Identify the blood parasite species.
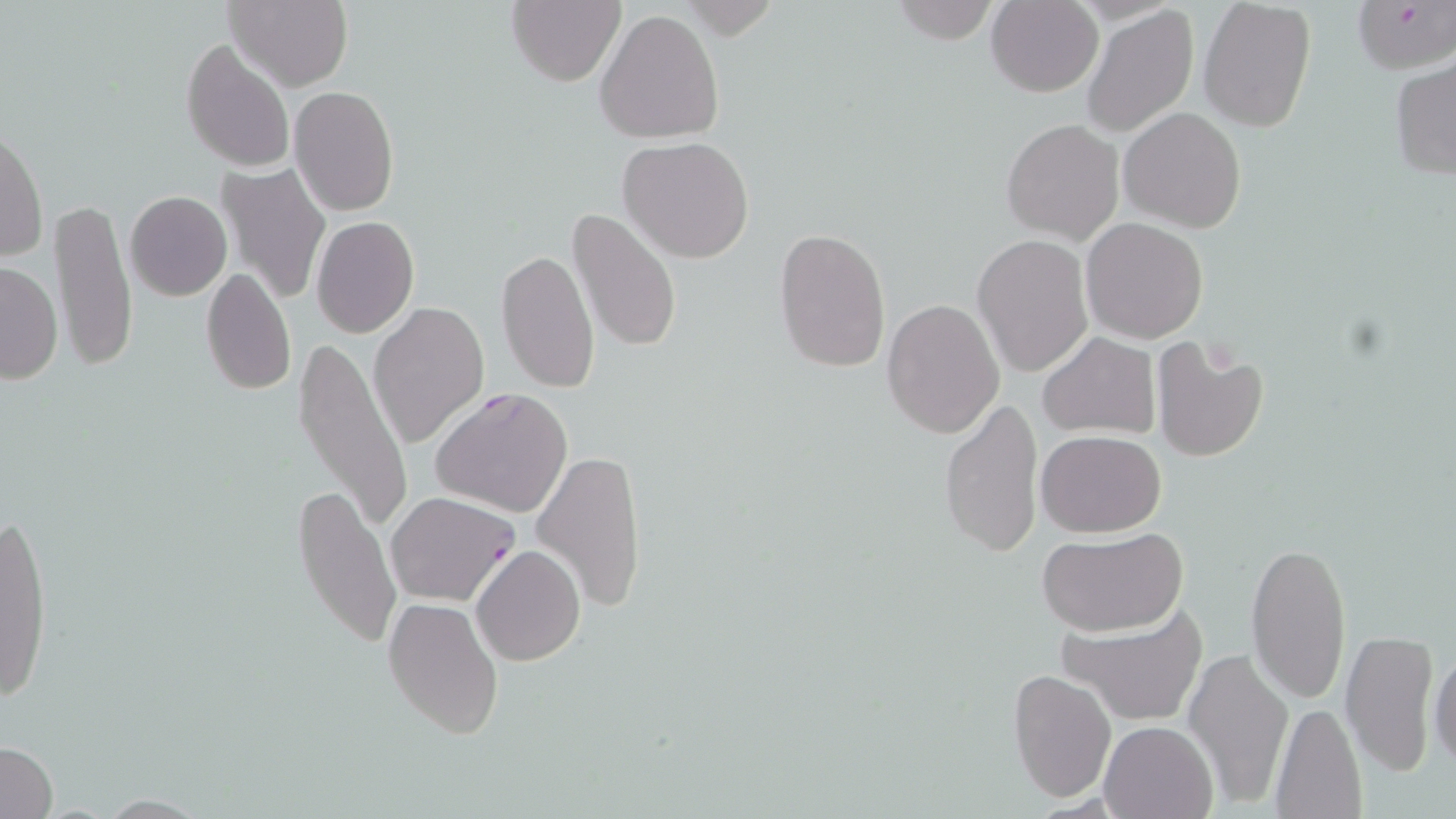
Plasmodium falciparum.

magnification = 1000x
field of view = single
image size = 1456×819 pixels
modality = light microscopy
stain = May-Grünwald-Giemsa
preparation = thin blood smear
Plasmodium falciparum-infected red blood cell locations = approximate bounding boxes as (x1,y1)-(x2,y2) corner pairs in pixels: (430,387)-(574,518), (385,491)-(520,607)
platelet locations = approximate bounding boxes as (x1,y1)-(x2,y2) corner pairs in pixels: (1201,343)-(1247,378)
uninfected red blood cell locations = approximate bounding boxes as (x1,y1)-(x2,y2) corner pairs in pixels: (224,0)-(352,92), (506,0)-(626,87), (1197,0)-(1316,132), (986,1)-(1103,97), (1353,1)-(1456,74), (888,2)-(999,44), (1080,4)-(1199,139), (593,8)-(725,145), (179,38)-(297,174), (1389,59)-(1456,180), (289,86)-(399,217), (1119,108)-(1246,232), (1001,118)-(1124,243), (1,126)-(47,264), (618,135)-(755,263), (215,164)-(332,306), (125,190)-(231,300), (51,198)-(137,375), (569,208)-(681,354), (310,215)-(420,338), (1082,219)-(1208,343), (773,227)-(890,374), (973,235)-(1093,377), (496,249)-(600,394), (2,261)-(63,385), (199,268)-(296,395), (881,297)-(1004,439), (370,300)-(489,450), (1037,331)-(1161,441), (296,334)-(416,534), (1150,336)-(1270,462), (939,397)-(1042,556), (1035,429)-(1167,536), (532,448)-(647,611), (291,480)-(402,653), (1,509)-(55,707), (1036,529)-(1186,637), (1245,538)-(1351,704), (472,544)-(586,667), (383,599)-(505,739), (1063,610)-(1204,724), (1339,631)-(1440,774), (1184,645)-(1295,806), (1428,650)-(1456,771), (1008,668)-(1117,802), (1269,702)-(1366,818), (1099,719)-(1220,818), (1,740)-(58,818)